Classify this cell by malaria status.
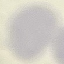
It is uninfected.

Summary:
  - Preparation: thin smear
  - Stain: Giemsa
  - Image type: cell patch, automatically extracted from a larger field of view and resized to 64 × 64 pixels
  - Capture: smartphone camera at the microscope eyepiece